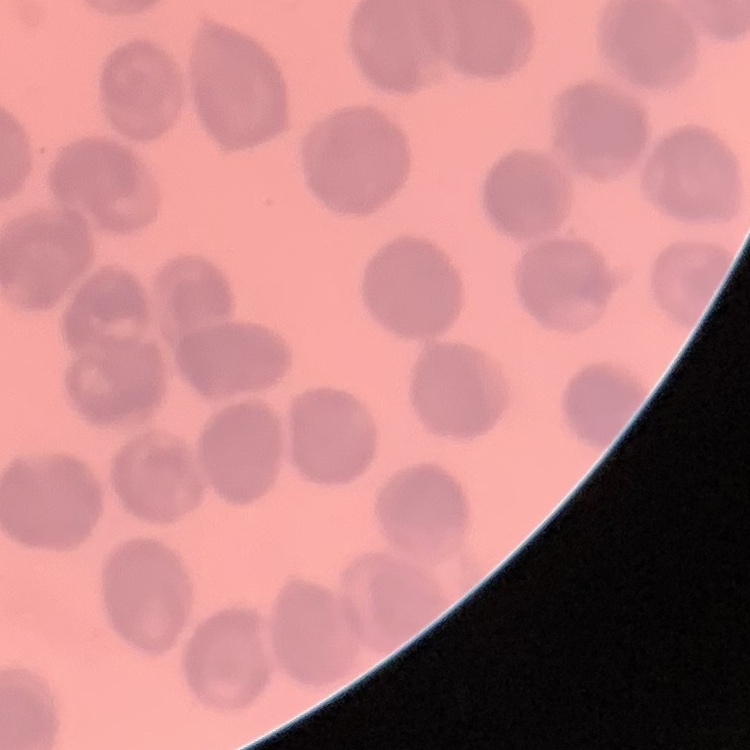
red_blood_cell_morphology: no rouleaux formation
stain: Field's or Giemsa
preparation: thin blood film
image_type: square crop of a larger photomicrograph